Report the malaria status of this cell.
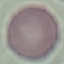

Uninfected.

Thin blood smear. Automatically extracted cell patch, resized to 64 × 64 pixels. Photographed with a smartphone camera at the microscope eyepiece. Giemsa stain.